Identify the parasite.
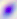

Toxoplasma gondii.

Micrograph. Captured at 400x magnification.